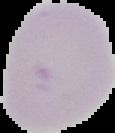
Cell region segmented out of the field of view; the surrounding area is masked to black. Image is 115×133 pixels. From a thin blood smear. Malaria status: uninfected.